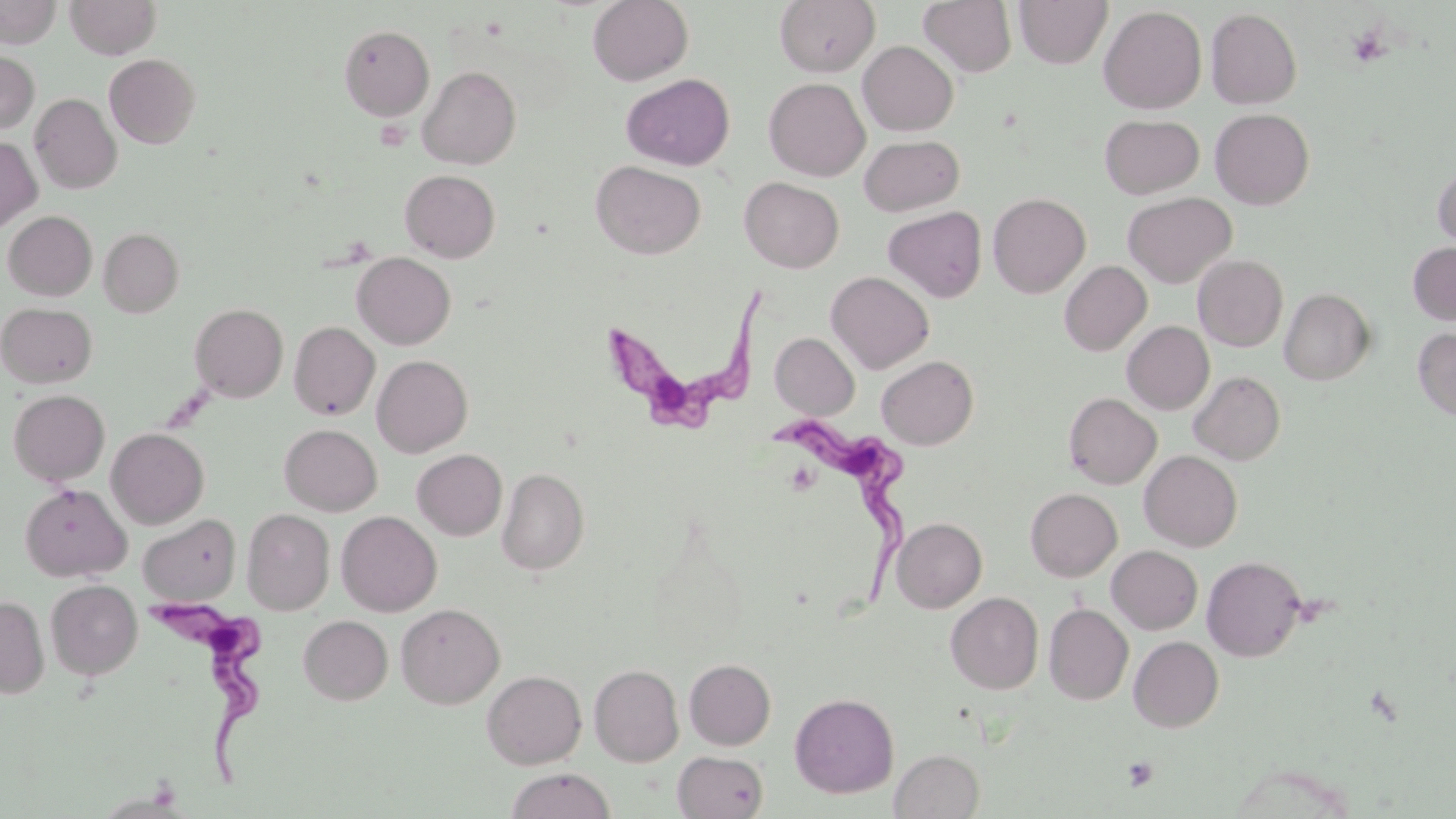 Approximate bounding boxes as named x1/y1/x2/y2 corners in pixels. Trypanosoma brucei locations: (x1=599, y1=288, x2=771, y2=446), (x1=764, y1=419, x2=917, y2=608), (x1=139, y1=586, x2=276, y2=789). Platelet locations: (x1=1347, y1=26, x2=1389, y2=68), (x1=1121, y1=756, x2=1159, y2=791). Uninfected red blood cell locations: (x1=0, y1=0, x2=61, y2=48), (x1=66, y1=0, x2=161, y2=59), (x1=587, y1=0, x2=693, y2=86), (x1=775, y1=0, x2=879, y2=77), (x1=919, y1=0, x2=1017, y2=77), (x1=1013, y1=0, x2=1113, y2=69), (x1=1099, y1=6, x2=1207, y2=114), (x1=1205, y1=8, x2=1302, y2=109), (x1=339, y1=25, x2=435, y2=121), (x1=858, y1=41, x2=958, y2=136), (x1=0, y1=49, x2=39, y2=133), (x1=104, y1=53, x2=200, y2=148), (x1=418, y1=66, x2=521, y2=169), (x1=621, y1=73, x2=735, y2=170), (x1=764, y1=78, x2=870, y2=181), (x1=30, y1=93, x2=121, y2=194), (x1=1210, y1=108, x2=1314, y2=209), (x1=1099, y1=114, x2=1205, y2=199), (x1=858, y1=135, x2=965, y2=216), (x1=0, y1=136, x2=42, y2=233), (x1=591, y1=161, x2=706, y2=259), (x1=1433, y1=162, x2=1456, y2=254), (x1=400, y1=170, x2=500, y2=262), (x1=739, y1=177, x2=844, y2=273), (x1=1122, y1=191, x2=1236, y2=288), (x1=988, y1=193, x2=1091, y2=297), (x1=883, y1=206, x2=986, y2=302), (x1=3, y1=211, x2=97, y2=300), (x1=99, y1=227, x2=184, y2=317), (x1=1408, y1=242, x2=1456, y2=325), (x1=352, y1=252, x2=455, y2=349), (x1=1193, y1=254, x2=1288, y2=352), (x1=1060, y1=261, x2=1152, y2=355), (x1=826, y1=271, x2=933, y2=373), (x1=1279, y1=288, x2=1376, y2=385), (x1=0, y1=302, x2=97, y2=388), (x1=190, y1=303, x2=288, y2=402), (x1=289, y1=321, x2=380, y2=420), (x1=1122, y1=321, x2=1214, y2=414), (x1=1412, y1=328, x2=1456, y2=420), (x1=770, y1=332, x2=860, y2=420), (x1=372, y1=355, x2=473, y2=457), (x1=877, y1=356, x2=978, y2=449), (x1=1189, y1=371, x2=1285, y2=464), (x1=8, y1=389, x2=110, y2=486), (x1=1063, y1=392, x2=1162, y2=489), (x1=280, y1=424, x2=381, y2=515), (x1=106, y1=427, x2=210, y2=528), (x1=412, y1=449, x2=507, y2=540), (x1=1139, y1=450, x2=1242, y2=551), (x1=497, y1=468, x2=589, y2=575), (x1=19, y1=482, x2=131, y2=582), (x1=1026, y1=488, x2=1122, y2=581), (x1=242, y1=509, x2=334, y2=615), (x1=336, y1=511, x2=442, y2=616), (x1=138, y1=514, x2=240, y2=604), (x1=891, y1=517, x2=987, y2=612), (x1=1107, y1=545, x2=1203, y2=634), (x1=1201, y1=556, x2=1306, y2=661), (x1=46, y1=579, x2=143, y2=679), (x1=946, y1=592, x2=1043, y2=693), (x1=0, y1=595, x2=48, y2=697), (x1=396, y1=603, x2=505, y2=709), (x1=1043, y1=603, x2=1133, y2=705), (x1=299, y1=615, x2=393, y2=704), (x1=1129, y1=636, x2=1223, y2=732), (x1=684, y1=659, x2=776, y2=750), (x1=589, y1=664, x2=684, y2=767), (x1=482, y1=670, x2=586, y2=769), (x1=789, y1=692, x2=899, y2=798), (x1=890, y1=749, x2=985, y2=818), (x1=672, y1=750, x2=769, y2=818), (x1=506, y1=768, x2=616, y2=819). Slide-level diagnosis: Trypanosoma brucei. Thin blood smear. May-Grünwald-Giemsa-stained preparation. Optical microscopy. Captured at 1000x magnification. Image is 1456×819 pixels. Single field of view.